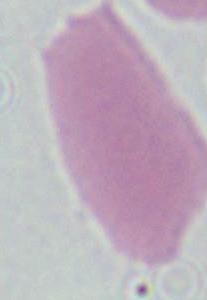
Summary:
  - Modality: micrograph
  - Identification: erythrocyte
  - Magnification: 1000x